Locate the cells, classifying each as a parasitized RBC, an uninfected RBC, or a WBC.
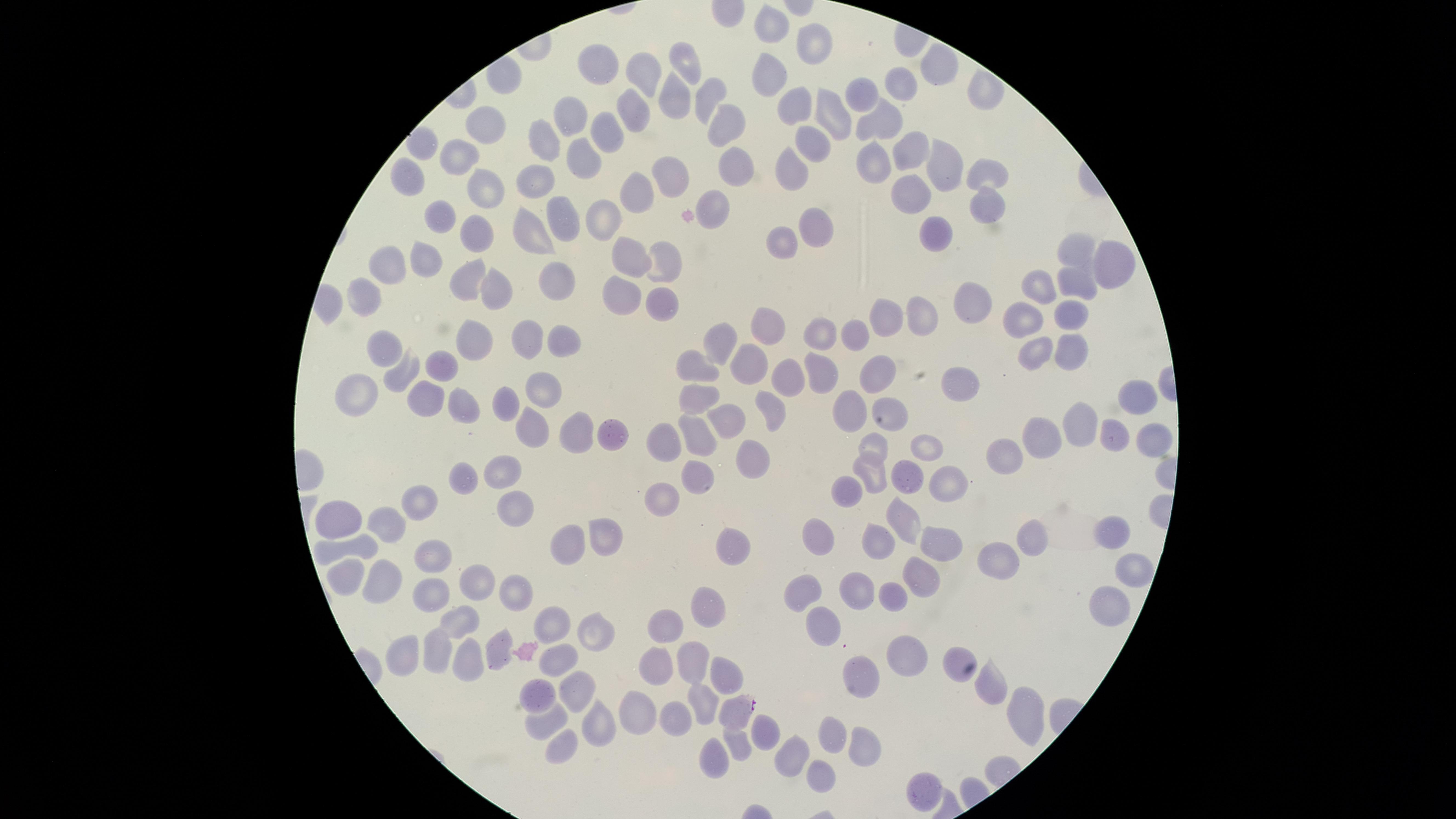
Approximate marker points as (x, y) in pixels.
Parasitized RBCs: (734, 711).
Uninfected RBCs: (775, 23), (805, 44), (688, 63), (594, 64), (932, 66), (770, 75), (643, 77), (903, 84), (979, 92), (706, 95), (863, 95), (672, 99), (796, 104), (833, 112), (569, 118), (634, 119), (874, 123), (726, 124), (607, 128), (483, 129), (540, 144), (815, 145), (419, 148), (908, 149), (585, 153), (456, 159), (942, 163), (870, 166), (733, 167), (788, 170), (982, 171), (672, 174), (405, 180), (535, 182), (482, 185), (633, 194), (907, 199), (714, 203), (986, 205), (559, 212), (599, 215), (439, 217), (814, 225), (530, 228), (466, 234), (929, 236), (779, 245), (1069, 252), (628, 257), (422, 259), (664, 261), (1107, 263), (382, 266), (548, 277), (1071, 280), (463, 282), (1034, 287), (497, 288), (362, 289), (619, 295), (659, 304), (973, 304), (1063, 314), (917, 316), (885, 321), (1022, 321), (767, 327), (856, 334), (816, 335), (474, 336), (525, 336), (568, 341), (715, 341), (384, 347), (1072, 351), (756, 356), (1032, 359), (702, 363), (441, 366), (819, 368), (874, 369), (398, 371), (783, 377), (953, 381), (540, 382), (355, 391), (427, 395), (1134, 397), (465, 400), (698, 400), (775, 405), (507, 406), (854, 406), (895, 407), (726, 416), (1068, 423), (527, 424), (615, 426), (576, 428), (699, 430), (664, 436), (1114, 436), (1037, 437), (1149, 440), (879, 443), (924, 446), (1004, 459), (748, 460), (507, 472), (871, 472), (904, 475), (951, 477), (465, 479), (695, 479), (845, 484), (665, 500), (431, 503), (513, 513), (349, 520), (391, 523), (900, 525), (1112, 530), (1029, 533), (607, 538), (881, 539), (817, 540), (733, 542), (941, 544), (335, 545), (566, 546), (430, 554), (998, 562), (354, 572), (1129, 572), (916, 578), (472, 579), (384, 581), (855, 586), (429, 592), (800, 592), (506, 595), (885, 597), (1099, 607), (707, 608), (460, 619), (816, 620), (549, 622), (590, 629), (667, 630), (497, 649), (437, 651), (956, 656), (405, 657), (903, 657), (471, 662), (555, 665), (690, 666), (654, 667), (865, 667), (720, 675), (991, 679), (536, 691), (571, 693), (703, 700), (638, 713), (543, 718), (678, 718), (1019, 719), (594, 728), (764, 728), (830, 735), (739, 741), (564, 742), (788, 751), (859, 752), (714, 757), (819, 772), (918, 789).
No WBCs identified.

Summary:
  - Preparation: thin blood film
  - Image size: 1456×819 pixels
  - Field of view: single
  - Species: Plasmodium falciparum
  - Stain: Giemsa
  - Capture: smartphone photograph through the microscope eyepiece
  - Visible region: circular